Name the parasite shown.
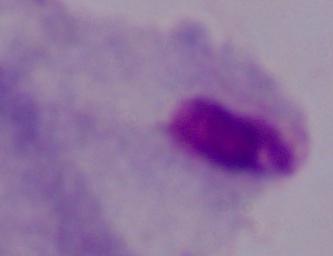

A trichomonad.

Captured at 1000x magnification. Photomicrograph.